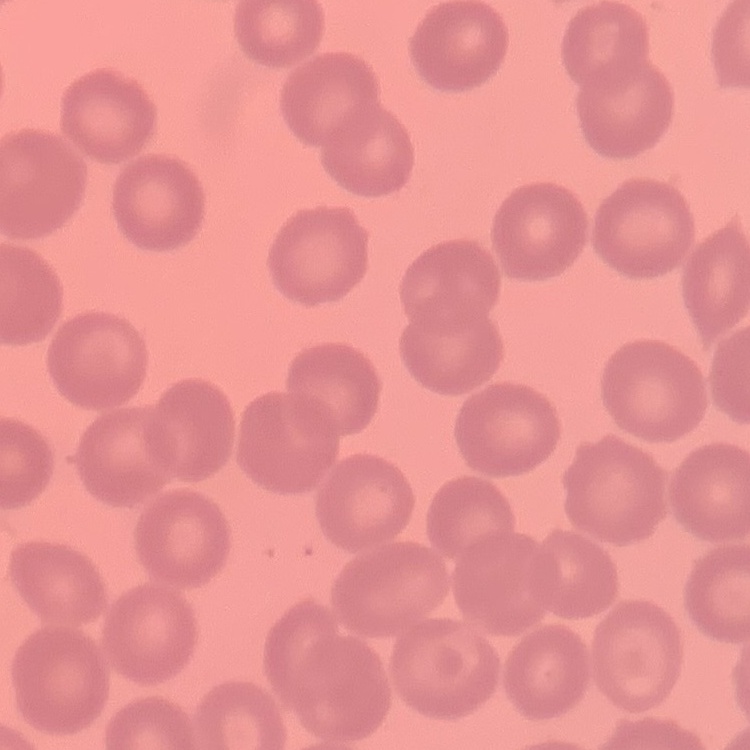
The erythrocytes show no rouleaux formation. Thin peripheral smear. Stained with either Field's or Giemsa. Square crop of a larger photomicrograph.